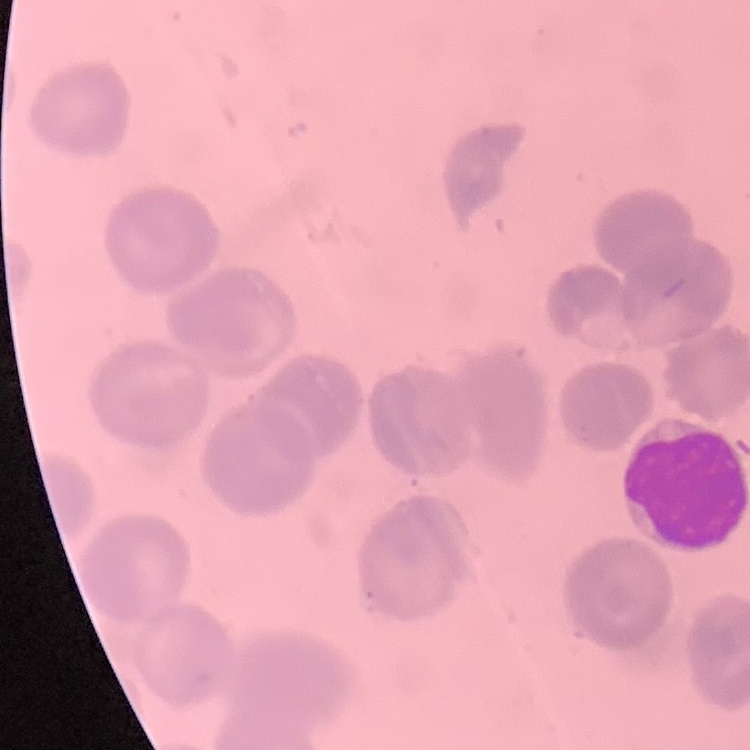

erythrocyte_morphology: no rouleaux formation
image_type: one tile cut from a larger photomicrograph
stain: Field's or Giemsa
preparation: thin blood smear